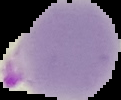

malaria status = parasitized
image type = segmented cell region on a black background
preparation = thin blood smear
image size = 121×100 pixels